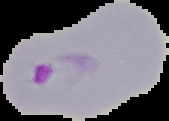

Summary:
  - Image size: 169×121 pixels
  - Preparation: thin blood smear
  - Image type: segmented cell region on a black background
  - Result: malaria parasites identified